Classify this cell by malaria status.
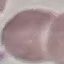

It is uninfected.

preparation = thin blood film
stain = Giemsa
image type = cell patch, automatically extracted from a larger field of view and resized to 64 × 64 pixels
capture = smartphone through the microscope eyepiece